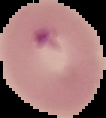
Segmented cell region on a black background. From a thin blood smear. Image is 106×118 pixels. Result: malaria parasites detected.